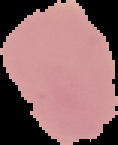
preparation = thin blood smear
malaria status = uninfected
image type = segmented cell region on a black background
image size = 118×145 pixels